Classify this cell by malaria status.
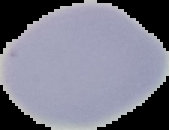
Uninfected.

Summary:
  - Image size: 169×130 pixels
  - Image type: segmented cell region with the area outside set to black
  - Preparation: thin blood film